Describe the morphology of the red blood cells.
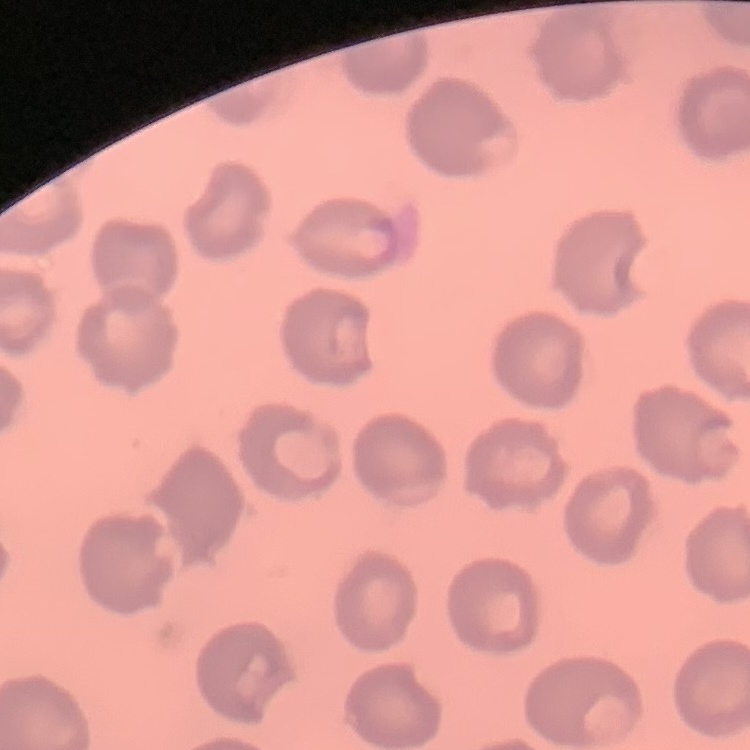

They show no rouleaux formation.

Field's or Giemsa stain. Square crop of a larger photomicrograph. Thin blood film.